Assess this cell for malaria.
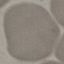
It is uninfected.

capture = smartphone through the microscope eyepiece
stain = Giemsa
image type = cell patch, automatically extracted from a larger field of view and resized to 64 × 64 pixels
preparation = thin blood film